Locate every blood parasite and identify its species.
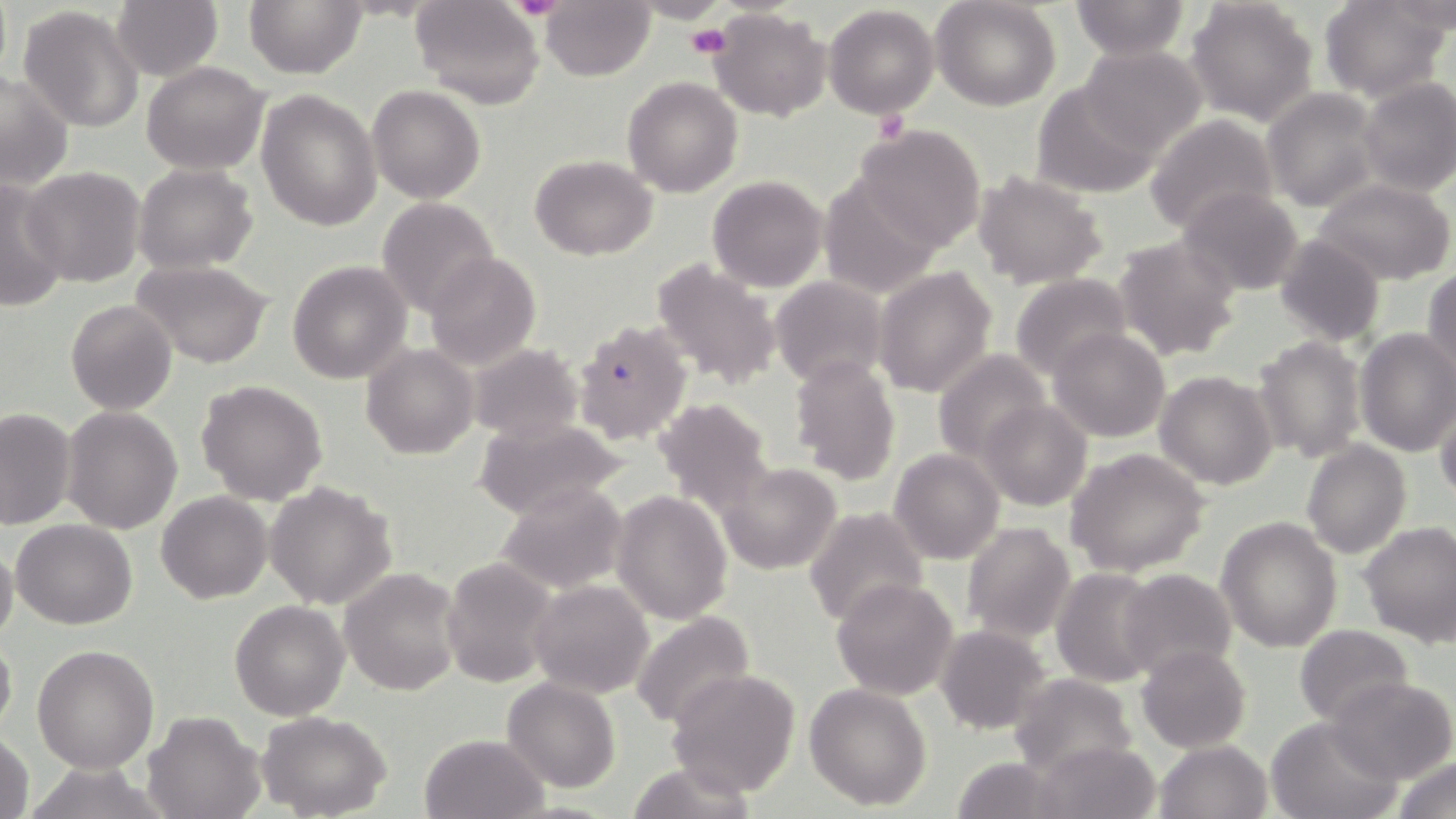

Approximate bounding boxes as named x1/y1/x2/y2 corners in pixels.
Plasmodium falciparum-infected red blood cells: (x1=571, y1=317, x2=692, y2=445).
No Plasmodium ovale, Plasmodium malariae, Plasmodium vivax, Babesia divergens, or Trypanosoma brucei observed.

Platelet locations: (x1=509, y1=0, x2=565, y2=19), (x1=686, y1=23, x2=732, y2=60), (x1=873, y1=111, x2=910, y2=143). Uninfected red blood cell locations: (x1=244, y1=0, x2=365, y2=78), (x1=412, y1=0, x2=545, y2=109), (x1=637, y1=0, x2=730, y2=25), (x1=932, y1=0, x2=1060, y2=111), (x1=1069, y1=1, x2=1192, y2=59), (x1=1186, y1=1, x2=1316, y2=126), (x1=1320, y1=1, x2=1449, y2=101), (x1=112, y1=2, x2=222, y2=81), (x1=541, y1=2, x2=654, y2=81), (x1=824, y1=4, x2=939, y2=117), (x1=18, y1=5, x2=145, y2=132), (x1=710, y1=9, x2=831, y2=121), (x1=1078, y1=45, x2=1206, y2=157), (x1=141, y1=61, x2=270, y2=175), (x1=0, y1=71, x2=74, y2=190), (x1=623, y1=76, x2=743, y2=198), (x1=1357, y1=77, x2=1455, y2=196), (x1=1031, y1=82, x2=1162, y2=200), (x1=367, y1=85, x2=485, y2=203), (x1=1262, y1=88, x2=1381, y2=211), (x1=257, y1=89, x2=383, y2=231), (x1=1144, y1=115, x2=1279, y2=235), (x1=852, y1=125, x2=986, y2=250), (x1=529, y1=155, x2=658, y2=258), (x1=132, y1=164, x2=257, y2=274), (x1=20, y1=166, x2=146, y2=287), (x1=974, y1=171, x2=1108, y2=288), (x1=817, y1=173, x2=946, y2=300), (x1=707, y1=175, x2=829, y2=292), (x1=0, y1=179, x2=70, y2=310), (x1=1315, y1=180, x2=1455, y2=285), (x1=1178, y1=186, x2=1305, y2=298), (x1=376, y1=197, x2=500, y2=319), (x1=1275, y1=233, x2=1387, y2=347), (x1=1111, y1=234, x2=1242, y2=364), (x1=424, y1=252, x2=540, y2=368), (x1=651, y1=258, x2=781, y2=390), (x1=133, y1=259, x2=274, y2=369), (x1=288, y1=261, x2=412, y2=384), (x1=875, y1=265, x2=999, y2=397), (x1=1424, y1=267, x2=1456, y2=381), (x1=1009, y1=274, x2=1132, y2=380), (x1=770, y1=276, x2=889, y2=389), (x1=65, y1=300, x2=177, y2=416), (x1=1048, y1=327, x2=1170, y2=443), (x1=1354, y1=329, x2=1456, y2=458), (x1=1253, y1=335, x2=1367, y2=465), (x1=362, y1=344, x2=479, y2=459), (x1=468, y1=344, x2=585, y2=442), (x1=933, y1=349, x2=1051, y2=463), (x1=789, y1=357, x2=900, y2=485), (x1=1154, y1=369, x2=1279, y2=490), (x1=197, y1=378, x2=328, y2=505), (x1=1434, y1=389, x2=1456, y2=502), (x1=650, y1=396, x2=775, y2=512), (x1=979, y1=399, x2=1092, y2=511), (x1=61, y1=406, x2=182, y2=533), (x1=0, y1=407, x2=76, y2=529), (x1=472, y1=418, x2=633, y2=520), (x1=1301, y1=440, x2=1411, y2=558), (x1=889, y1=448, x2=1005, y2=565), (x1=1066, y1=448, x2=1210, y2=575), (x1=717, y1=462, x2=843, y2=575), (x1=762, y1=479, x2=893, y2=614), (x1=265, y1=480, x2=399, y2=611), (x1=494, y1=483, x2=628, y2=594), (x1=157, y1=491, x2=271, y2=604), (x1=612, y1=491, x2=732, y2=623), (x1=804, y1=507, x2=928, y2=627), (x1=1216, y1=516, x2=1344, y2=652), (x1=11, y1=520, x2=137, y2=630), (x1=960, y1=520, x2=1076, y2=644), (x1=1358, y1=520, x2=1456, y2=645), (x1=0, y1=543, x2=19, y2=650), (x1=440, y1=558, x2=560, y2=687), (x1=340, y1=567, x2=462, y2=696), (x1=1050, y1=567, x2=1162, y2=687), (x1=1116, y1=568, x2=1237, y2=681), (x1=829, y1=577, x2=959, y2=701), (x1=529, y1=580, x2=654, y2=698), (x1=229, y1=601, x2=349, y2=721), (x1=630, y1=612, x2=755, y2=731), (x1=1294, y1=623, x2=1413, y2=727), (x1=935, y1=625, x2=1052, y2=733), (x1=0, y1=631, x2=17, y2=739), (x1=32, y1=644, x2=160, y2=773), (x1=1135, y1=645, x2=1252, y2=752), (x1=666, y1=667, x2=802, y2=796), (x1=1009, y1=673, x2=1136, y2=779), (x1=1329, y1=677, x2=1455, y2=783), (x1=503, y1=678, x2=620, y2=792), (x1=804, y1=683, x2=932, y2=810), (x1=144, y1=710, x2=265, y2=819), (x1=257, y1=711, x2=392, y2=818), (x1=1266, y1=716, x2=1401, y2=819), (x1=0, y1=730, x2=35, y2=819), (x1=419, y1=733, x2=550, y2=819), (x1=1034, y1=739, x2=1162, y2=819), (x1=1154, y1=739, x2=1272, y2=819), (x1=1389, y1=754, x2=1456, y2=819), (x1=948, y1=756, x2=1065, y2=819), (x1=623, y1=761, x2=758, y2=818). Slide-level diagnosis: Plasmodium falciparum. May-Grünwald-Giemsa stain. Image is 1456×819 pixels. Thin blood smear. Optical microscopy. Single field of view. 1000x magnification.